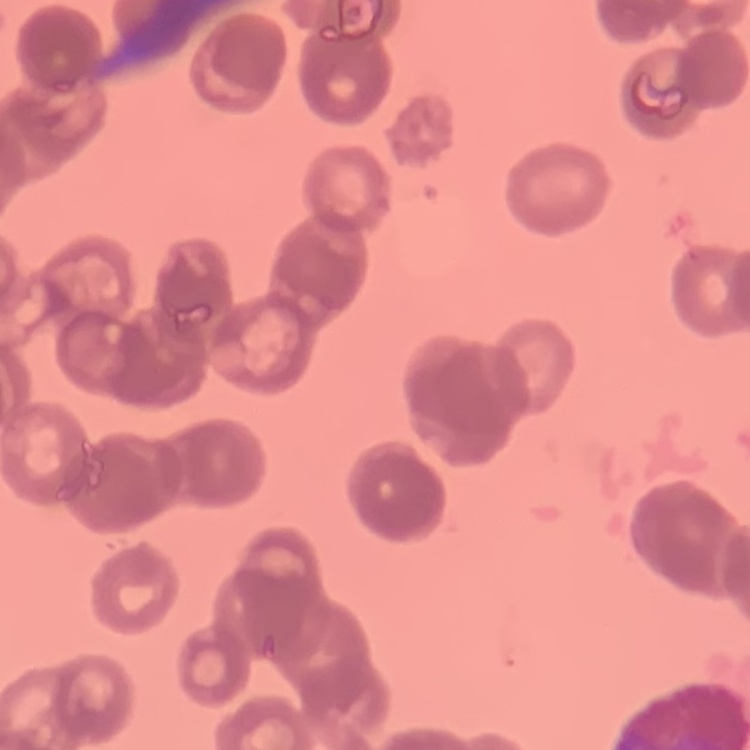
{
  "red_blood_cell_morphology": "rouleaux formation",
  "stain": "Field's or Giemsa",
  "preparation": "thin blood smear",
  "image_type": "square crop of a larger photomicrograph"
}